Outline each blood parasite and name the species.
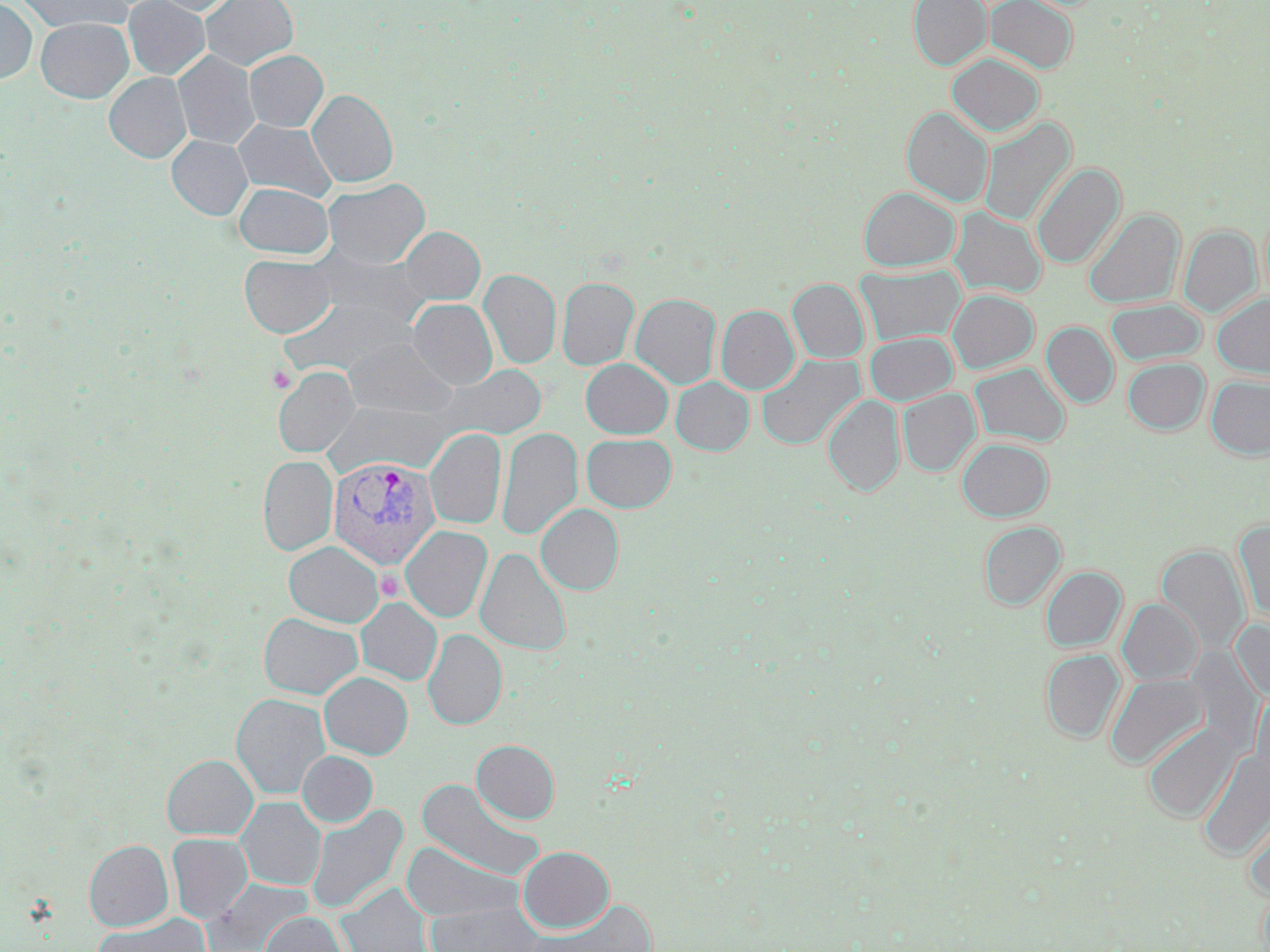

Approximate bounding boxes as [x1, y1, x2, y2] in pixels.
Plasmodium vivax-infected red blood cells: [328, 457, 441, 569].
No Plasmodium falciparum, Plasmodium ovale, Plasmodium malariae, Babesia divergens, or Trypanosoma brucei observed.

Summary:
  - Platelet locations: [267, 365, 296, 392], [377, 569, 403, 600]
  - Uninfected red blood cell locations: [0, 0, 37, 84], [16, 0, 132, 33], [123, 0, 210, 79], [150, 0, 237, 15], [201, 0, 298, 71], [908, 0, 990, 70], [985, 0, 1078, 73], [35, 18, 132, 103], [244, 50, 328, 132], [173, 52, 260, 149], [947, 53, 1044, 136], [105, 72, 191, 162], [307, 89, 398, 187], [902, 107, 993, 207], [979, 118, 1075, 226], [233, 120, 336, 201], [167, 135, 252, 220], [1031, 162, 1125, 269], [322, 178, 429, 268], [234, 183, 332, 258], [859, 187, 959, 271], [949, 207, 1046, 298], [1083, 209, 1183, 308], [1179, 225, 1260, 318], [399, 227, 485, 305], [311, 249, 431, 331], [239, 255, 336, 337], [856, 264, 964, 346], [479, 269, 561, 369], [557, 276, 639, 370], [788, 279, 869, 363], [947, 289, 1038, 374], [631, 293, 721, 389], [1213, 294, 1270, 377], [281, 295, 414, 377], [407, 299, 497, 389], [1106, 299, 1206, 366], [716, 305, 799, 394], [1042, 323, 1118, 407], [865, 332, 957, 405], [343, 340, 457, 418], [756, 354, 864, 450], [1123, 358, 1209, 435], [581, 359, 673, 439], [970, 363, 1070, 447], [441, 365, 547, 440], [273, 366, 360, 457], [1206, 376, 1270, 459], [671, 377, 753, 455], [898, 388, 980, 476], [823, 395, 905, 496], [322, 400, 451, 477], [496, 427, 582, 540], [425, 428, 507, 529], [582, 434, 677, 512], [957, 438, 1052, 521], [258, 456, 337, 555], [536, 504, 623, 594], [1233, 520, 1270, 623], [979, 522, 1066, 609], [401, 526, 492, 622], [283, 541, 384, 627], [1157, 545, 1249, 656], [475, 548, 571, 655], [1041, 566, 1126, 652], [356, 598, 442, 685], [1118, 599, 1202, 685], [258, 613, 362, 699], [1231, 617, 1270, 704], [423, 629, 507, 729], [1041, 649, 1124, 743], [319, 672, 413, 759], [1105, 673, 1208, 770], [1250, 688, 1270, 793], [231, 693, 331, 799], [1143, 722, 1237, 822], [472, 740, 560, 823], [1197, 748, 1270, 861], [297, 750, 377, 827], [161, 754, 258, 839], [415, 778, 546, 881], [236, 797, 325, 891], [1241, 803, 1270, 900], [306, 804, 407, 915], [167, 833, 253, 923], [84, 840, 173, 931], [400, 842, 523, 922], [517, 846, 614, 933], [205, 878, 312, 952], [337, 883, 433, 952], [529, 900, 657, 951], [425, 902, 544, 951], [95, 911, 210, 952], [260, 912, 348, 952]
  - Slide-level diagnosis: Plasmodium vivax
  - Preparation: thin blood film
  - Stain: May-Grünwald-Giemsa
  - Modality: light microscopy
  - Magnification: 1000x
  - Field of view: single
  - Image size: 1270×952 pixels